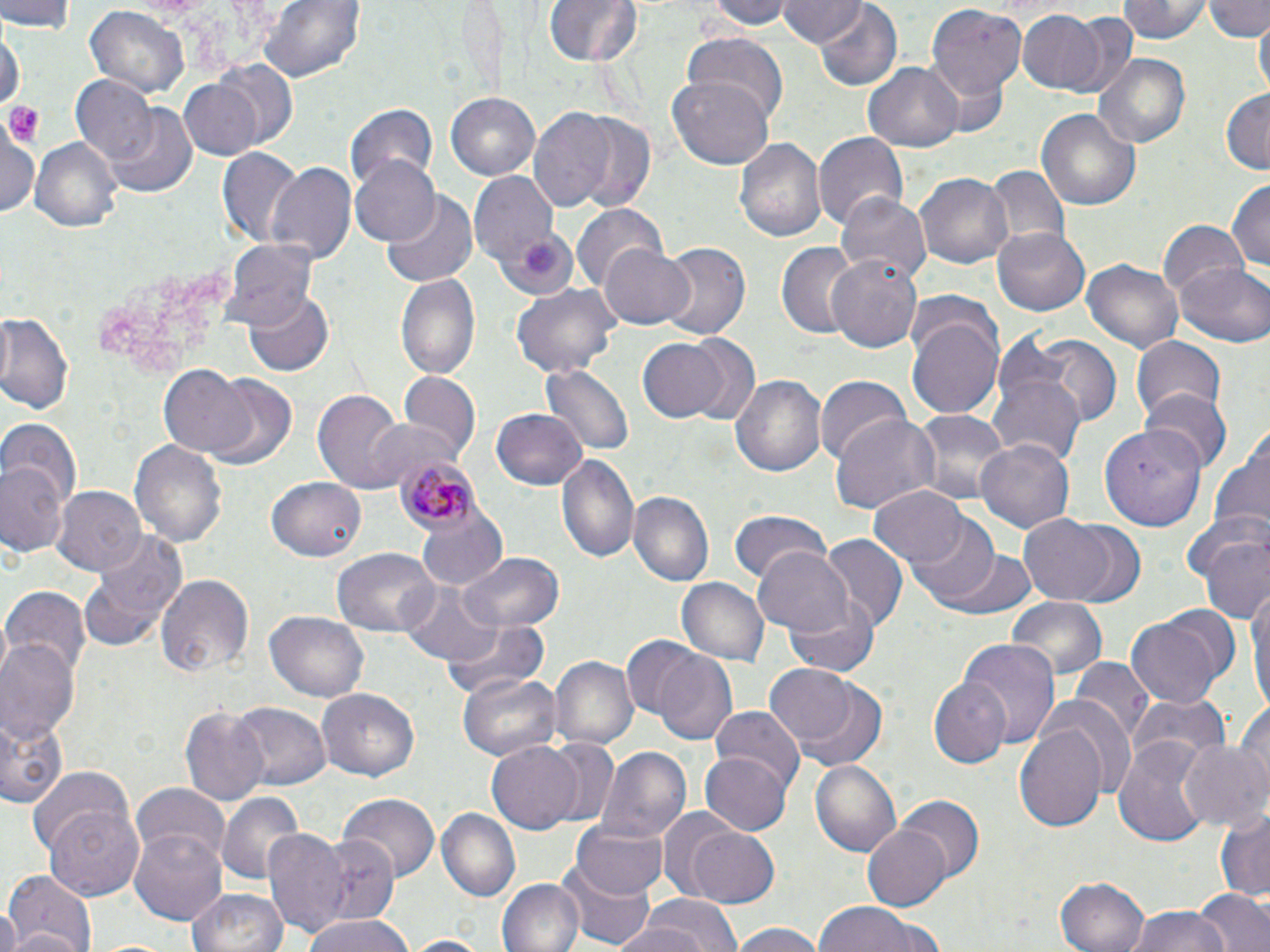

Summary:
  - Coordinate format: approximate bounding boxes as named x1/y1/x2/y2 corners in pixels
  - Platelet locations: (x1=6, y1=103, x2=44, y2=146)
  - Plasmodium malariae-infected red blood cell locations: (x1=396, y1=454, x2=477, y2=532)
  - Uninfected red blood cell locations: (x1=1, y1=0, x2=78, y2=34), (x1=257, y1=0, x2=365, y2=86), (x1=544, y1=0, x2=640, y2=69), (x1=707, y1=0, x2=797, y2=30), (x1=1120, y1=0, x2=1214, y2=44), (x1=1202, y1=0, x2=1270, y2=40), (x1=774, y1=1, x2=865, y2=49), (x1=85, y1=4, x2=189, y2=98), (x1=811, y1=4, x2=903, y2=89), (x1=927, y1=5, x2=1027, y2=104), (x1=1018, y1=10, x2=1107, y2=93), (x1=1056, y1=12, x2=1137, y2=96), (x1=1254, y1=17, x2=1269, y2=95), (x1=0, y1=27, x2=24, y2=109), (x1=682, y1=34, x2=788, y2=120), (x1=1093, y1=54, x2=1194, y2=150), (x1=209, y1=59, x2=300, y2=150), (x1=862, y1=62, x2=964, y2=151), (x1=177, y1=77, x2=265, y2=160), (x1=667, y1=77, x2=774, y2=170), (x1=73, y1=78, x2=160, y2=166), (x1=1221, y1=89, x2=1270, y2=173), (x1=447, y1=92, x2=543, y2=180), (x1=345, y1=101, x2=439, y2=190), (x1=104, y1=105, x2=199, y2=200), (x1=528, y1=105, x2=652, y2=214), (x1=1036, y1=109, x2=1142, y2=212), (x1=2, y1=129, x2=42, y2=217), (x1=815, y1=134, x2=908, y2=231), (x1=734, y1=136, x2=826, y2=243), (x1=31, y1=138, x2=123, y2=234), (x1=218, y1=149, x2=303, y2=248), (x1=351, y1=154, x2=442, y2=247), (x1=264, y1=162, x2=355, y2=268), (x1=985, y1=167, x2=1067, y2=255), (x1=469, y1=173, x2=561, y2=269), (x1=915, y1=174, x2=1013, y2=270), (x1=1227, y1=178, x2=1270, y2=274), (x1=382, y1=193, x2=479, y2=288), (x1=839, y1=193, x2=930, y2=285), (x1=574, y1=203, x2=668, y2=294), (x1=1158, y1=221, x2=1247, y2=303), (x1=992, y1=225, x2=1090, y2=314), (x1=498, y1=231, x2=577, y2=298), (x1=221, y1=240, x2=320, y2=330), (x1=656, y1=240, x2=752, y2=340), (x1=775, y1=241, x2=859, y2=338), (x1=599, y1=242, x2=695, y2=329), (x1=825, y1=254, x2=924, y2=355), (x1=1083, y1=261, x2=1182, y2=353), (x1=1175, y1=263, x2=1270, y2=346), (x1=395, y1=273, x2=482, y2=383), (x1=510, y1=282, x2=621, y2=376), (x1=243, y1=289, x2=333, y2=376), (x1=906, y1=307, x2=1005, y2=419), (x1=0, y1=311, x2=74, y2=415), (x1=1005, y1=333, x2=1120, y2=429), (x1=635, y1=335, x2=743, y2=425), (x1=1131, y1=336, x2=1226, y2=422), (x1=160, y1=365, x2=253, y2=458), (x1=542, y1=365, x2=636, y2=452), (x1=203, y1=374, x2=298, y2=469), (x1=396, y1=374, x2=480, y2=464), (x1=732, y1=376, x2=826, y2=477), (x1=990, y1=376, x2=1086, y2=469), (x1=816, y1=378, x2=911, y2=466), (x1=314, y1=389, x2=407, y2=495), (x1=1140, y1=390, x2=1229, y2=473), (x1=491, y1=407, x2=589, y2=490), (x1=912, y1=410, x2=1007, y2=506), (x1=831, y1=415, x2=939, y2=516), (x1=366, y1=417, x2=453, y2=491), (x1=2, y1=418, x2=82, y2=510), (x1=1209, y1=420, x2=1270, y2=546), (x1=1098, y1=426, x2=1207, y2=531), (x1=977, y1=439, x2=1073, y2=535), (x1=130, y1=440, x2=228, y2=548), (x1=554, y1=452, x2=641, y2=566), (x1=0, y1=461, x2=67, y2=560), (x1=267, y1=477, x2=369, y2=561), (x1=53, y1=486, x2=147, y2=577), (x1=870, y1=486, x2=972, y2=570), (x1=628, y1=491, x2=715, y2=588), (x1=415, y1=506, x2=509, y2=591), (x1=730, y1=511, x2=832, y2=588), (x1=1018, y1=514, x2=1123, y2=606), (x1=909, y1=517, x2=1000, y2=605), (x1=1187, y1=519, x2=1270, y2=623), (x1=1062, y1=520, x2=1145, y2=603), (x1=78, y1=531, x2=186, y2=650), (x1=820, y1=535, x2=908, y2=630), (x1=753, y1=546, x2=855, y2=636), (x1=331, y1=547, x2=439, y2=637), (x1=454, y1=551, x2=565, y2=634), (x1=941, y1=551, x2=1038, y2=619), (x1=156, y1=574, x2=255, y2=679), (x1=677, y1=578, x2=767, y2=666), (x1=400, y1=579, x2=501, y2=664), (x1=3, y1=587, x2=91, y2=677), (x1=1248, y1=589, x2=1270, y2=712), (x1=785, y1=593, x2=882, y2=676), (x1=1006, y1=599, x2=1108, y2=686), (x1=266, y1=609, x2=370, y2=701), (x1=1123, y1=614, x2=1227, y2=709), (x1=444, y1=619, x2=548, y2=703), (x1=0, y1=636, x2=80, y2=746), (x1=621, y1=636, x2=706, y2=724), (x1=958, y1=639, x2=1060, y2=752), (x1=651, y1=649, x2=735, y2=743), (x1=550, y1=656, x2=638, y2=752), (x1=1069, y1=659, x2=1154, y2=739), (x1=766, y1=663, x2=862, y2=750), (x1=458, y1=673, x2=561, y2=762), (x1=788, y1=675, x2=888, y2=769), (x1=931, y1=675, x2=1014, y2=769), (x1=317, y1=689, x2=419, y2=782), (x1=1130, y1=695, x2=1231, y2=773), (x1=1233, y1=699, x2=1270, y2=804), (x1=232, y1=702, x2=333, y2=790), (x1=181, y1=708, x2=270, y2=808), (x1=709, y1=708, x2=804, y2=799), (x1=0, y1=715, x2=68, y2=810), (x1=1013, y1=723, x2=1107, y2=833), (x1=539, y1=737, x2=621, y2=827), (x1=1113, y1=739, x2=1213, y2=846), (x1=1177, y1=739, x2=1269, y2=836), (x1=486, y1=741, x2=584, y2=833), (x1=598, y1=748, x2=691, y2=843), (x1=700, y1=753, x2=791, y2=834), (x1=811, y1=760, x2=902, y2=854), (x1=25, y1=764, x2=137, y2=859), (x1=131, y1=782, x2=229, y2=865), (x1=218, y1=791, x2=305, y2=888), (x1=339, y1=795, x2=438, y2=885), (x1=898, y1=797, x2=985, y2=882), (x1=44, y1=805, x2=145, y2=901), (x1=437, y1=807, x2=520, y2=901), (x1=657, y1=807, x2=745, y2=897), (x1=1215, y1=808, x2=1270, y2=904), (x1=571, y1=820, x2=669, y2=900), (x1=863, y1=823, x2=952, y2=912), (x1=299, y1=827, x2=402, y2=934), (x1=686, y1=827, x2=780, y2=907), (x1=263, y1=829, x2=353, y2=941), (x1=130, y1=831, x2=224, y2=924), (x1=4, y1=870, x2=100, y2=951), (x1=564, y1=871, x2=656, y2=947), (x1=1056, y1=874, x2=1148, y2=952), (x1=499, y1=877, x2=583, y2=952), (x1=186, y1=887, x2=289, y2=952), (x1=1194, y1=889, x2=1270, y2=952), (x1=640, y1=894, x2=740, y2=951), (x1=812, y1=901, x2=944, y2=952), (x1=1127, y1=906, x2=1235, y2=952), (x1=0, y1=909, x2=22, y2=952), (x1=302, y1=914, x2=411, y2=952), (x1=727, y1=921, x2=826, y2=952), (x1=601, y1=922, x2=715, y2=952), (x1=402, y1=936, x2=490, y2=952)
  - Slide-level diagnosis: Plasmodium malariae
  - Stain: May-Grünwald-Giemsa
  - Magnification: 1000x
  - Image size: 1270×952 pixels
  - Preparation: thin blood film
  - Modality: optical microscopy
  - Field of view: one of a larger specimen